Locate every Plasmodium parasite.
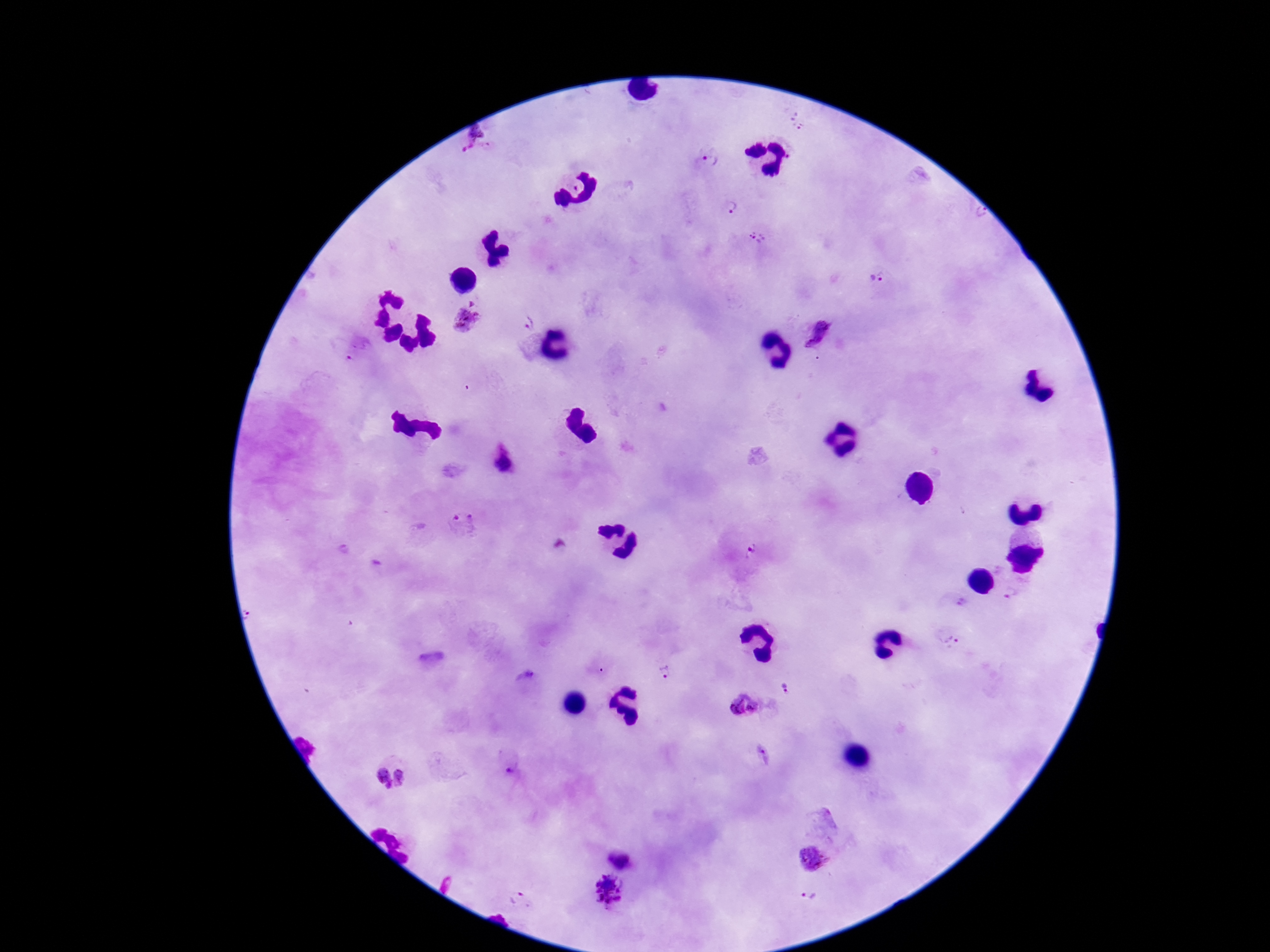

Approximate centers as [x, y] in pixels.
Plasmodium parasites: [800, 126], [474, 141], [710, 161], [727, 205], [979, 215], [757, 238], [879, 277], [468, 318], [527, 325], [816, 335], [502, 464], [462, 519], [750, 550], [346, 551], [1010, 592], [949, 640], [665, 670], [525, 677], [786, 688], [744, 705], [512, 768], [400, 777], [383, 779], [622, 855], [813, 858], [610, 890], [808, 897], [517, 898].

Summary:
  - Image size: 1270×952 pixels
  - Preparation: thick peripheral-blood smear
  - Capture: smartphone camera through the microscope eyepiece
  - Field of view: single
  - Magnification: 100x
  - Stain: Giemsa
  - Patient malaria status: positive